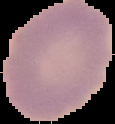

{
  "image_type": "segmented cell region on a black background",
  "preparation": "thin blood film",
  "image_size": "115×124 pixels",
  "result": "negative for Plasmodium parasites"
}